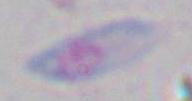
Summary:
  - Magnification: 1000x
  - Identification: Toxoplasma gondii
  - Modality: photomicrograph